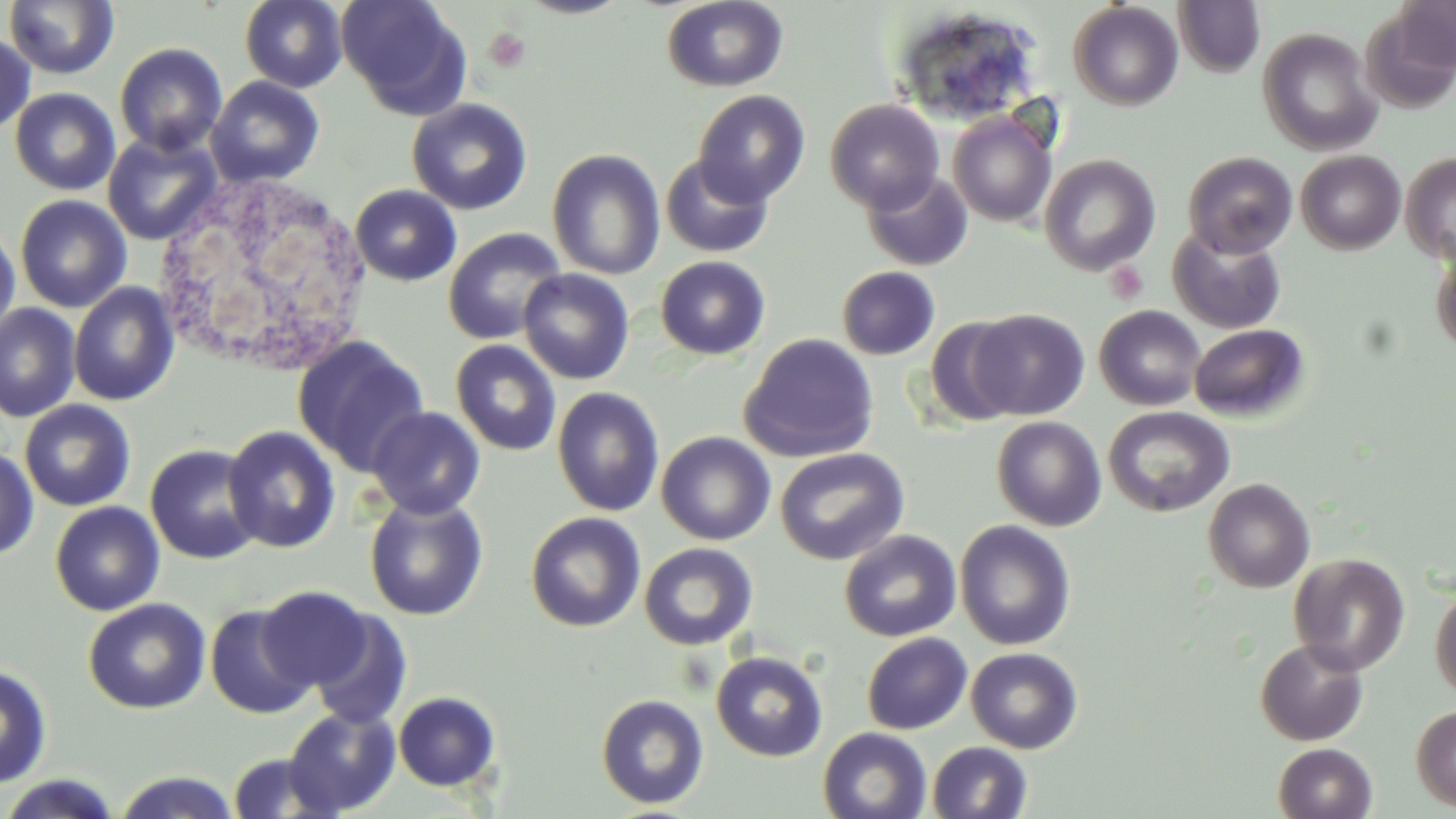
slide-level diagnosis = no evidence of blood parasites
platelet locations = approximate bounding boxes as [x1, y1, x2, y2] in pixels: [483, 27, 531, 74], [1105, 261, 1148, 303]
preparation = thin blood film
field of view = single
magnification = 1000x
image size = 1456×819 pixels
modality = light microscopy
uninfected red blood cell locations = approximate bounding boxes as [x1, y1, x2, y2] in pixels: [240, 0, 347, 92], [336, 0, 472, 119], [515, 0, 632, 19], [661, 0, 788, 92], [1395, 0, 1455, 78], [3, 1, 119, 80], [1172, 1, 1265, 78], [1068, 2, 1183, 111], [892, 8, 1044, 127], [1258, 27, 1382, 156], [0, 33, 36, 136], [114, 42, 228, 156], [206, 76, 325, 187], [10, 88, 120, 195], [692, 90, 811, 207], [407, 98, 532, 215], [825, 99, 944, 213], [948, 111, 1058, 227], [102, 131, 222, 245], [547, 149, 665, 280], [1296, 150, 1406, 254], [1183, 151, 1298, 257], [1401, 152, 1456, 265], [659, 154, 774, 258], [1039, 154, 1161, 276], [861, 169, 973, 271], [350, 185, 462, 286], [15, 194, 132, 313], [0, 222, 20, 338], [1167, 227, 1286, 334], [443, 228, 567, 344], [1431, 247, 1456, 357], [655, 255, 770, 360], [836, 266, 940, 360], [518, 269, 635, 384], [69, 282, 179, 406], [0, 303, 80, 422], [1094, 305, 1206, 411], [967, 309, 1090, 420], [923, 316, 1024, 428], [1189, 324, 1309, 421], [740, 333, 879, 463], [292, 335, 430, 475], [451, 339, 561, 456], [552, 386, 665, 517], [20, 399, 136, 511], [1103, 405, 1234, 517], [367, 406, 485, 519], [991, 416, 1107, 531], [222, 424, 341, 553], [656, 431, 776, 546], [145, 444, 264, 564], [0, 447, 38, 561], [775, 447, 909, 565], [1203, 478, 1315, 593], [363, 494, 488, 620], [50, 501, 165, 615], [526, 512, 645, 632], [955, 520, 1076, 651], [839, 529, 962, 642], [639, 542, 758, 651], [1288, 553, 1410, 675], [1430, 585, 1456, 701], [256, 586, 370, 690], [83, 598, 211, 714], [205, 603, 316, 719], [306, 607, 413, 730], [861, 633, 973, 734], [1255, 638, 1369, 746], [965, 647, 1083, 753], [711, 651, 828, 761], [0, 663, 52, 789], [393, 691, 501, 791], [596, 694, 709, 809], [1411, 704, 1456, 813], [282, 705, 401, 817], [818, 727, 932, 819], [927, 741, 1033, 819], [1274, 742, 1377, 819], [226, 751, 342, 818], [111, 770, 242, 819], [0, 774, 125, 818]
stain = May-Grünwald-Giemsa
white blood cell locations = approximate bounding boxes as [x1, y1, x2, y2] in pixels: [150, 168, 375, 376]